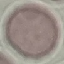
Summary:
  - Malaria status: uninfected
  - Image type: automatically extracted cell patch, resized to 64 × 64 pixels
  - Capture: smartphone through the microscope eyepiece
  - Preparation: thin blood film
  - Stain: Giemsa